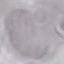

Summary:
  - Result: no malaria parasites seen
  - Image type: automatically extracted cell patch, resized to 64 × 64 pixels
  - Capture: smartphone camera at the microscope eyepiece
  - Preparation: thin smear
  - Stain: Giemsa